Give the position of every malaria parasite.
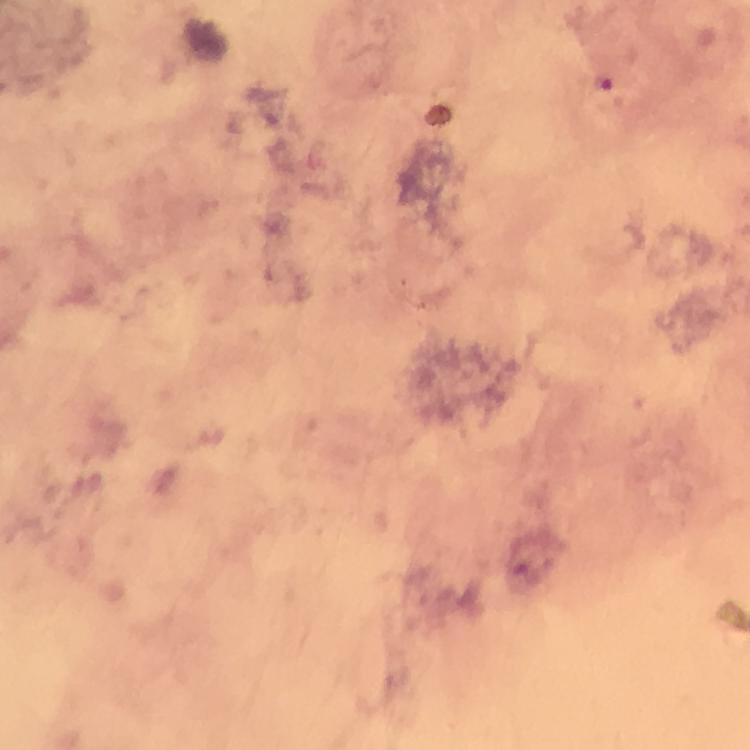
Approximate centers as (x, y) in pixels.
Malaria parasites: (605, 81).

cropped from = one field of view
context = from a diagnostic examination for malaria
magnification = 100x
image size = 750×750 pixels
preparation = thick blood film
capture = smartphone photograph through a microscope
stain = Giemsa
immersion oil = applied